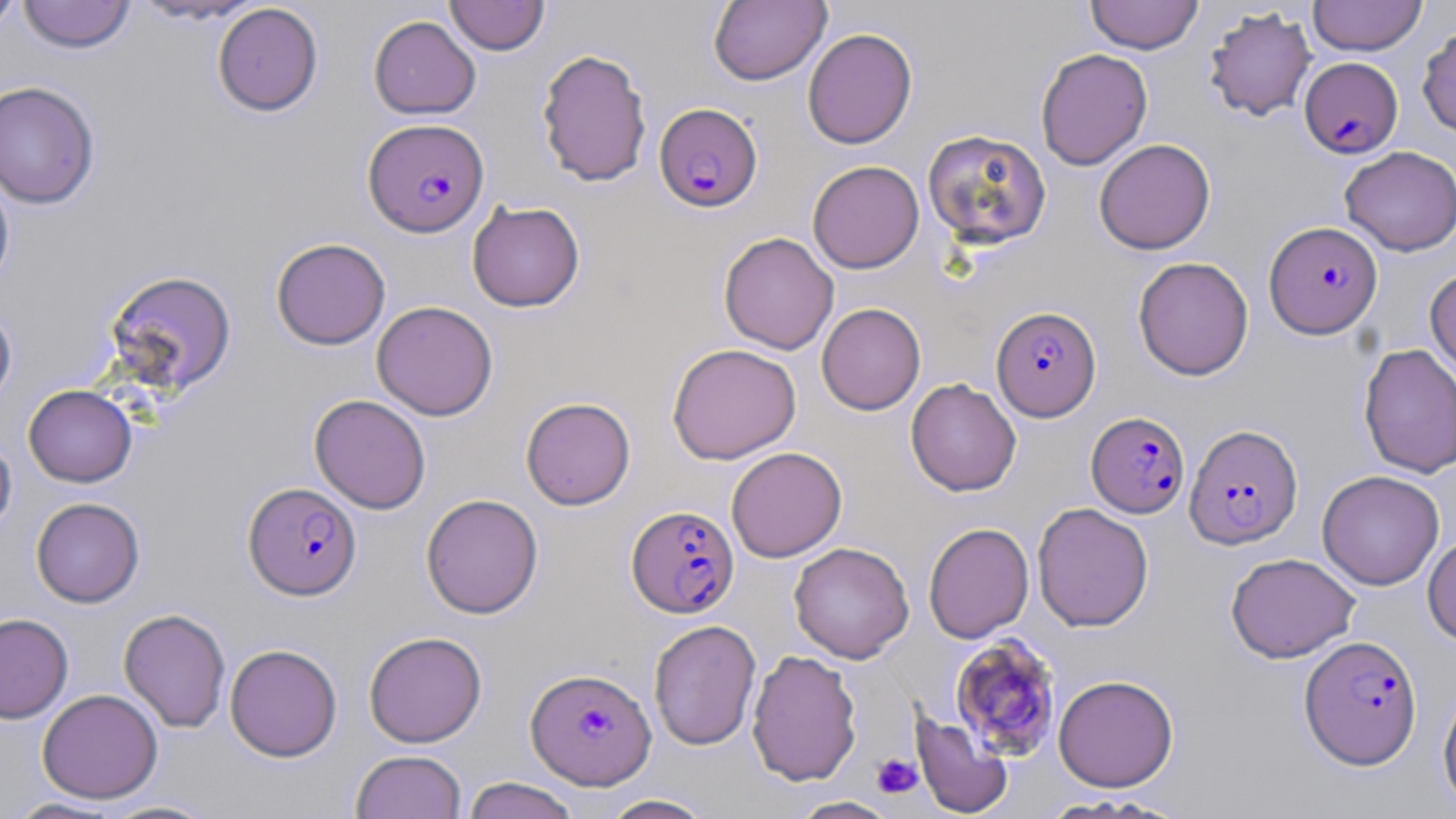
Summary:
  - Coordinate format: approximate bounding boxes as [x1, y1, x2, y2] in pixels
  - Platelet locations: [872, 753, 922, 798]
  - Uninfected red blood cell locations: [0, 0, 22, 37], [18, 0, 136, 54], [128, 0, 266, 26], [445, 0, 550, 55], [709, 0, 831, 86], [1085, 0, 1202, 54], [1308, 0, 1427, 56], [212, 3, 324, 117], [1203, 6, 1317, 122], [368, 15, 481, 119], [1417, 24, 1456, 138], [802, 27, 918, 149], [536, 48, 652, 187], [1035, 48, 1153, 170], [0, 80, 100, 209], [922, 129, 1052, 249], [1094, 138, 1216, 254], [1340, 146, 1456, 256], [807, 160, 924, 273], [0, 168, 15, 290], [467, 201, 585, 312], [718, 232, 839, 354], [271, 237, 391, 350], [1133, 256, 1254, 380], [1424, 268, 1456, 381], [105, 269, 237, 396], [372, 300, 498, 420], [0, 303, 17, 411], [817, 303, 926, 415], [667, 343, 801, 464], [1358, 343, 1456, 478], [905, 378, 1021, 496], [23, 384, 137, 487], [309, 394, 431, 514], [521, 397, 636, 510], [0, 437, 17, 540], [726, 446, 846, 562], [1316, 470, 1444, 590], [420, 493, 543, 618], [31, 497, 145, 607], [1032, 502, 1154, 631], [923, 522, 1034, 643], [1423, 533, 1456, 648], [788, 542, 914, 663], [1226, 552, 1359, 663], [118, 608, 231, 733], [0, 613, 73, 724], [648, 619, 761, 751], [363, 631, 487, 747], [224, 643, 342, 762], [747, 649, 862, 786], [1053, 674, 1179, 792], [1438, 682, 1456, 812], [37, 688, 163, 803], [910, 710, 1013, 818], [350, 750, 466, 819], [461, 776, 582, 819], [599, 794, 715, 819], [1035, 795, 1180, 818], [787, 796, 901, 818], [5, 797, 127, 818], [97, 798, 223, 818]
  - Plasmodium falciparum-infected red blood cell locations: [1299, 57, 1402, 158], [654, 103, 762, 212], [363, 117, 489, 237], [1264, 221, 1383, 338], [991, 305, 1101, 421], [1086, 411, 1190, 518], [1184, 423, 1303, 549], [243, 481, 361, 600], [626, 505, 739, 618], [1300, 635, 1422, 769], [943, 637, 1058, 763], [526, 668, 656, 788]
  - Slide-level diagnosis: Plasmodium falciparum
  - Stain: May-Grünwald-Giemsa
  - Field of view: single
  - Modality: light microscopy
  - Image size: 1456×819 pixels
  - Magnification: 1000x
  - Preparation: thin blood film